Assess the morphology of the red blood cells.
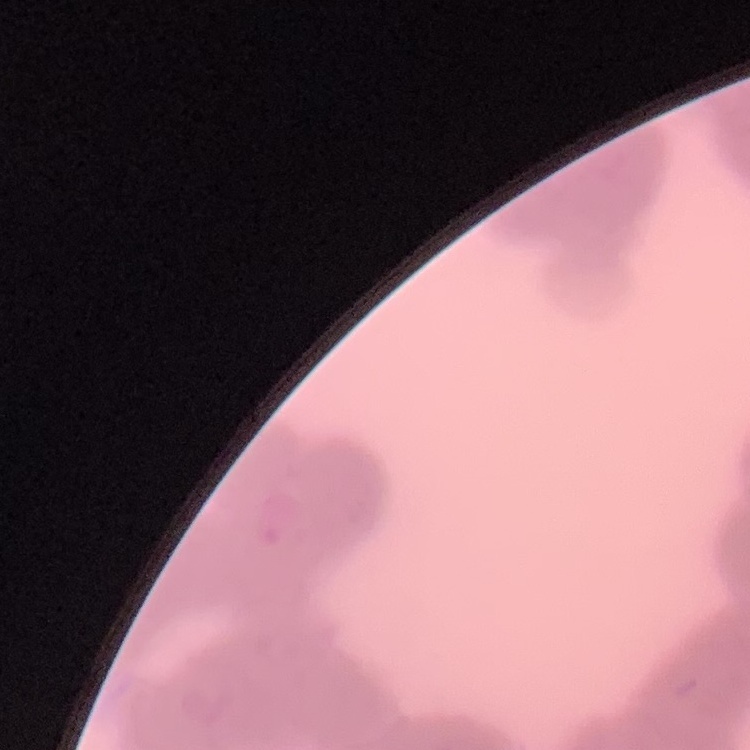
Rouleaux formation.

Thin blood smear. Square crop of a larger photomicrograph. Stained with either Field's or Giemsa.